Assess this cell for malaria.
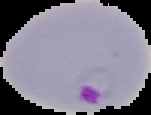

It is parasitized.

From a thin blood film. The area outside the segmented cell region is set to black. Image is 151×115 pixels.